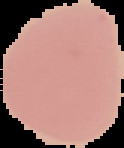

preparation = thin blood film
image size = 124×148 pixels
image type = cell region segmented out of the field of view; surrounding area masked to black
result = no Plasmodium parasites seen